Outline platelets.
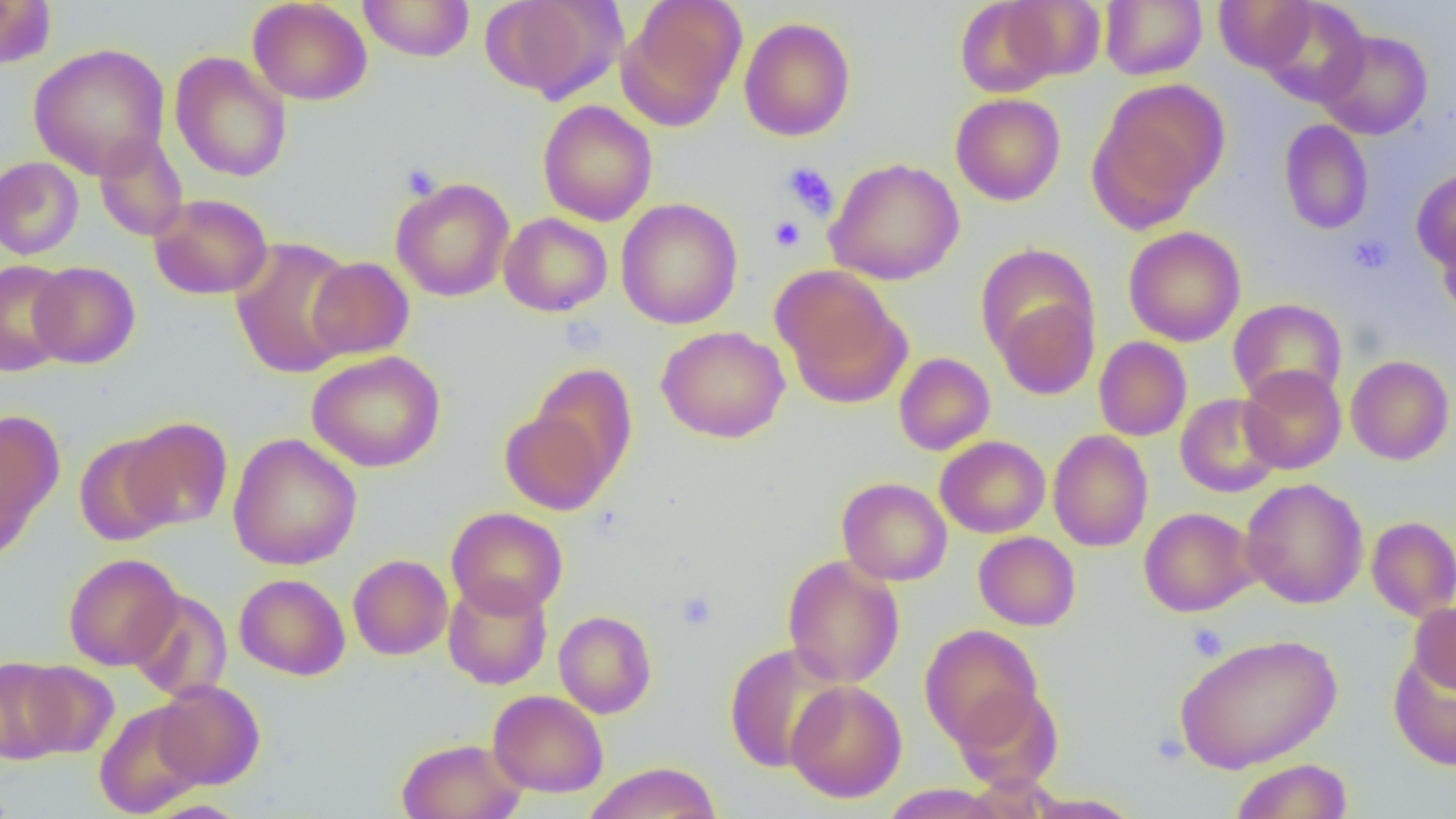
Approximate bounding boxes as (x1,y1)-(x2,y2) corner pairs in pixels.
Platelets: (781,162)-(839,220), (401,164)-(440,199), (769,216)-(805,251), (1348,233)-(1394,275), (675,591)-(718,631), (1188,623)-(1228,661).

{
  "slide_level_diagnosis": "negative for blood parasites",
  "preparation": "thin blood film",
  "modality": "optical microscopy",
  "magnification": "1000x",
  "uninfected_red_blood_cell_locations": "approximate bounding boxes as (x1,y1)-(x2,y2) corner pairs in pixels: (247,0)-(373,106), (358,0)-(475,62), (481,0)-(623,102), (954,0)-(1068,99), (997,0)-(1107,83), (1099,0)-(1207,80), (1214,0)-(1317,73), (0,1)-(54,70), (620,1)-(746,128), (1257,1)-(1370,107), (1097,2)-(1216,162), (739,16)-(856,142), (1315,29)-(1433,140), (28,42)-(170,179), (170,51)-(291,183), (1089,80)-(1229,226), (951,93)-(1066,206), (538,100)-(657,226), (1279,119)-(1374,235), (93,133)-(189,242), (0,157)-(83,260), (825,157)-(965,285), (1412,168)-(1456,271), (390,177)-(515,302), (148,193)-(273,300), (616,198)-(743,330), (499,212)-(612,317), (1437,217)-(1456,327), (1123,226)-(1246,346), (230,237)-(359,379), (975,243)-(1097,367), (306,256)-(415,360), (0,260)-(74,376), (30,261)-(140,368), (771,266)-(910,407), (993,295)-(1099,399), (1228,297)-(1347,406), (657,325)-(790,443), (1094,336)-(1192,441), (306,350)-(446,472), (894,352)-(994,456), (1346,355)-(1455,465), (529,364)-(638,485), (1238,365)-(1347,474), (1175,393)-(1284,498), (499,407)-(616,515), (0,409)-(63,553), (121,417)-(232,531), (1048,430)-(1153,552), (73,433)-(180,547), (227,433)-(362,571), (935,435)-(1051,538), (837,477)-(952,586), (1240,478)-(1368,608), (446,507)-(568,618), (1139,507)-(1258,617), (1366,515)-(1456,621), (973,531)-(1080,630), (63,553)-(182,670), (348,554)-(453,660), (781,555)-(905,688), (235,574)-(350,681), (442,577)-(553,690), (126,588)-(232,702), (442,594)-(655,698), (1409,602)-(1456,694), (553,610)-(657,719), (919,624)-(1043,749), (1174,632)-(1342,773), (724,643)-(845,772), (1388,650)-(1455,770), (0,656)-(74,764), (18,660)-(119,759), (153,679)-(265,789), (785,679)-(908,803), (951,685)-(1065,791), (487,690)-(609,797), (94,701)-(207,818), (396,737)-(527,819), (1229,759)-(1354,819), (584,761)-(722,819), (880,784)-(1007,819), (1026,792)-(1142,818)",
  "image_size": "1456×819 pixels",
  "field_of_view": "one of a larger specimen"
}